Give the preparation type.
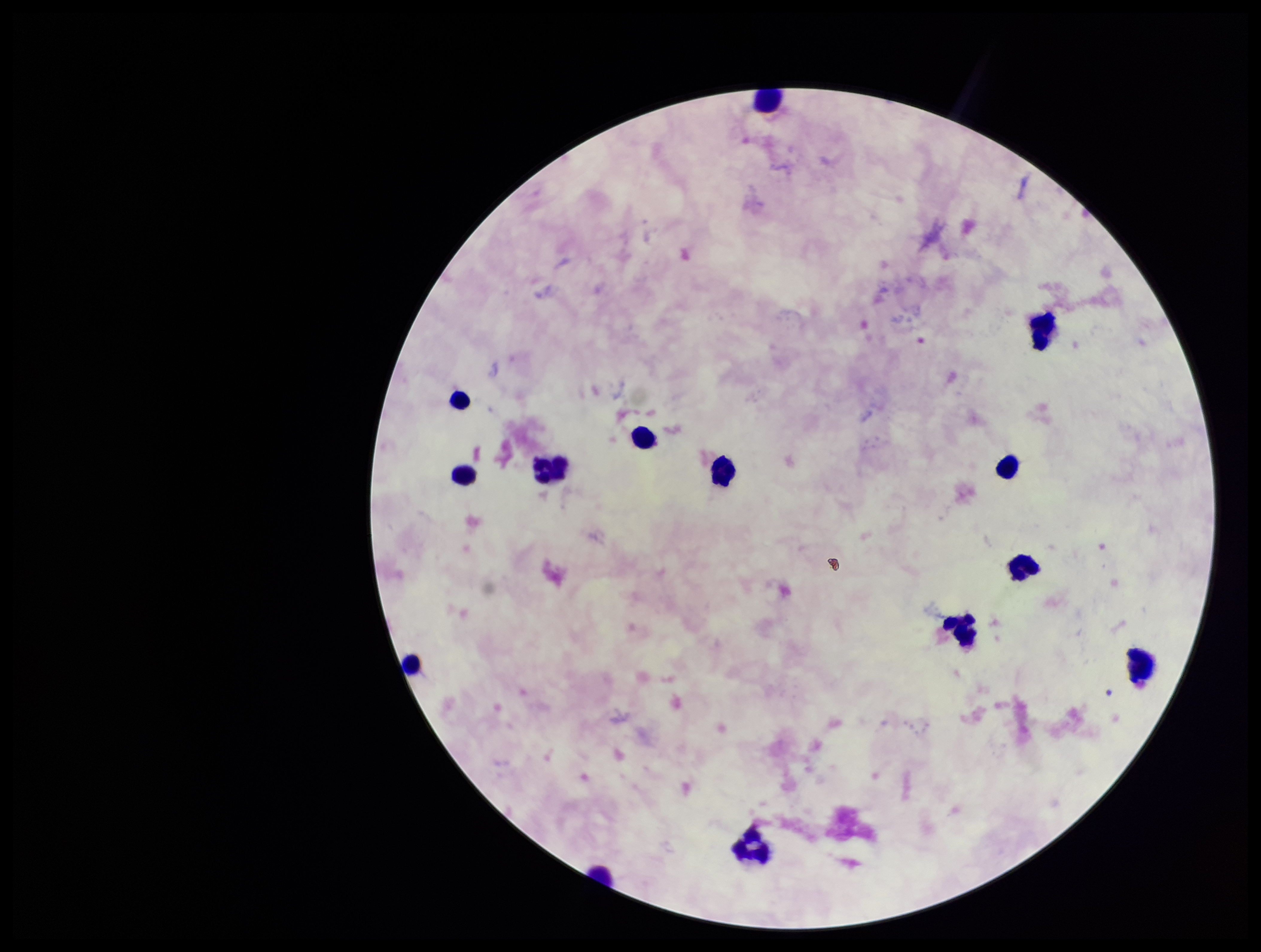

A thick smear.

Smartphone photograph taken through the eyepiece of a microscope. Parasite count: 0. Patient malaria status: negative. Image is 1261×952 pixels. Plasmodium parasites: none seen. One field from this slide. Stained with Giemsa. Leukocyte count: 13.